Describe the morphology of the red blood cells.
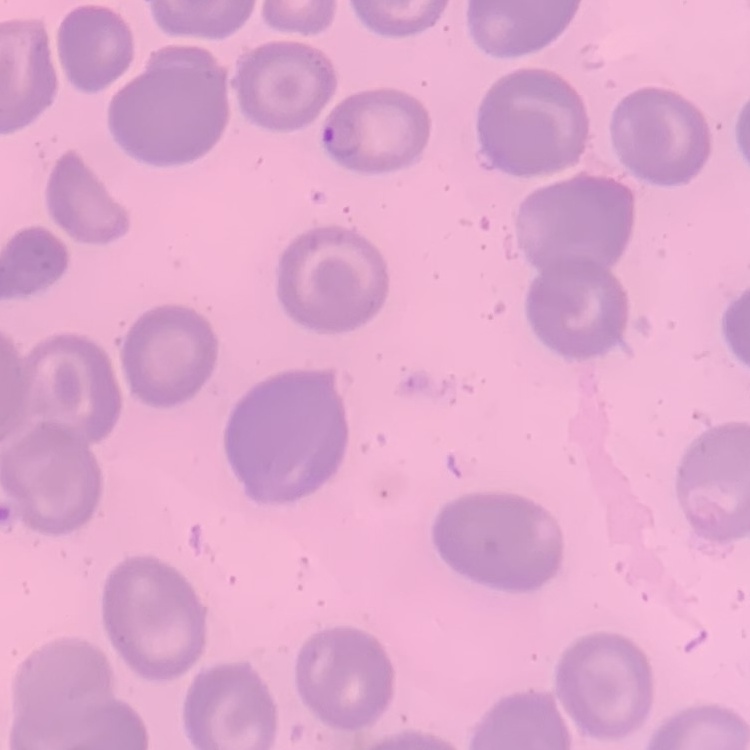
No rouleaux formation.

stain: Field's or Giemsa
image_type: square crop of a larger photomicrograph
preparation: thin blood smear